Outline each uninfected red blood cell.
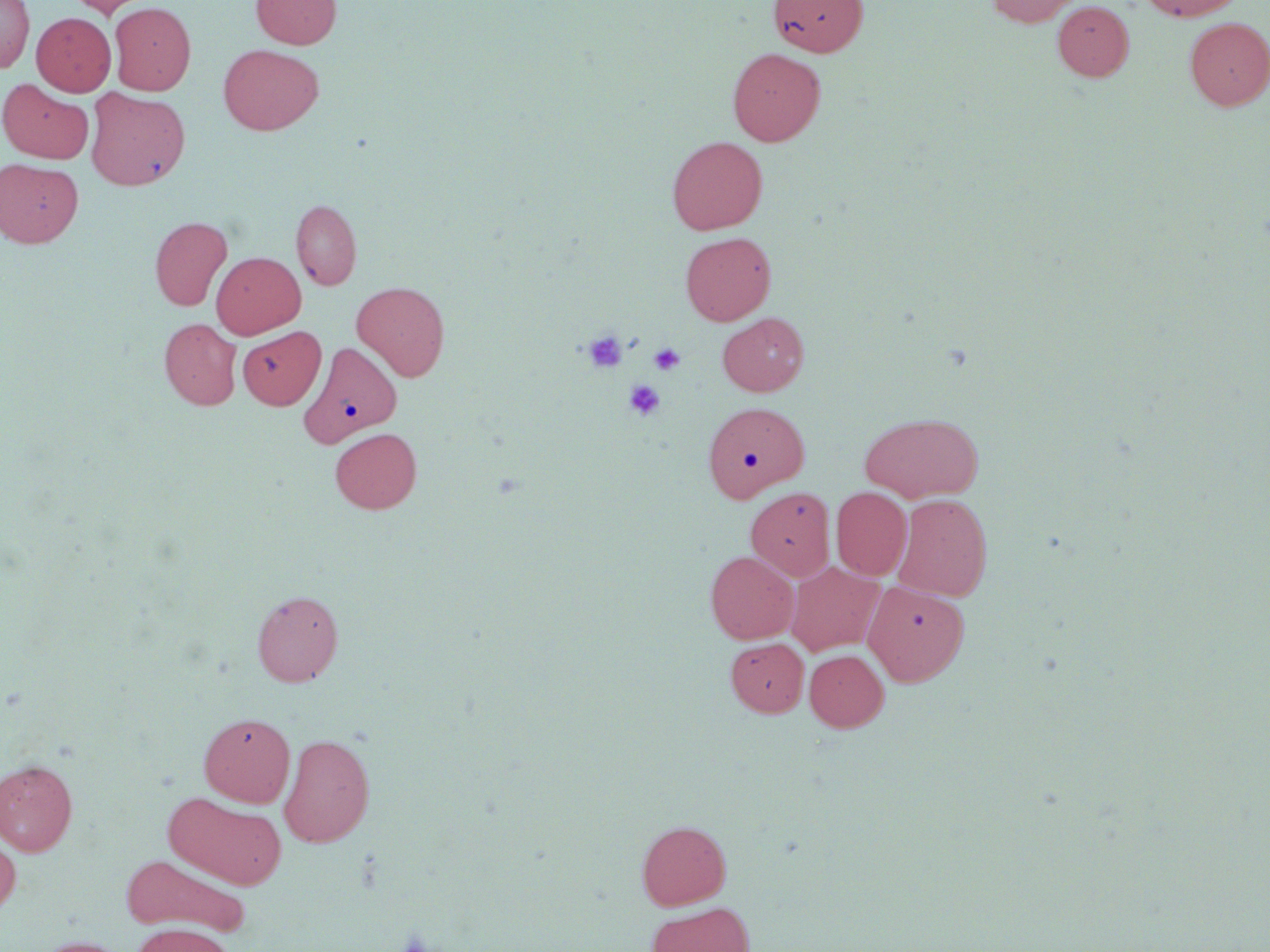
Approximate bounding boxes as [x1, y1, x2, y2] in pixels.
Uninfected red blood cells: [0, 0, 34, 72], [67, 0, 151, 18], [250, 0, 341, 49], [769, 0, 868, 56], [985, 0, 1081, 27], [1138, 0, 1244, 21], [1052, 1, 1134, 81], [109, 2, 196, 95], [32, 12, 116, 96], [1184, 17, 1270, 111], [218, 44, 324, 135], [727, 48, 826, 146], [0, 80, 94, 164], [86, 88, 190, 191], [667, 136, 768, 235], [0, 158, 83, 248], [291, 198, 362, 291], [150, 216, 232, 311], [680, 232, 776, 325], [211, 252, 305, 339], [352, 281, 450, 381], [718, 313, 808, 396], [159, 318, 241, 410], [237, 326, 325, 410], [301, 342, 402, 446], [703, 402, 809, 501], [859, 412, 983, 502], [330, 427, 422, 514], [746, 487, 835, 581], [831, 487, 911, 580], [893, 494, 993, 601], [706, 551, 799, 643], [786, 561, 884, 656], [863, 580, 969, 686], [252, 590, 343, 686], [726, 638, 809, 717], [805, 650, 888, 731], [199, 712, 295, 807], [279, 732, 375, 848], [0, 760, 78, 856], [165, 792, 287, 890], [637, 820, 731, 910], [0, 833, 20, 917], [121, 854, 248, 936], [646, 902, 755, 952], [132, 924, 233, 952], [30, 936, 132, 952].

Summary:
  - Platelet locations: [584, 332, 627, 372], [649, 343, 685, 376], [624, 380, 665, 420]
  - Slide-level diagnosis: no evidence of blood parasites
  - Preparation: thin blood smear
  - Field of view: one of a larger specimen
  - Magnification: 1000x
  - Image size: 1270×952 pixels
  - Modality: light microscopy
  - Stain: May-Grünwald-Giemsa